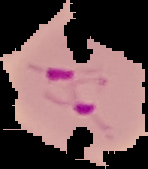 From a thin blood smear. Segmented cell region on a black background. Image is 148×169 pixels. Result: malaria parasites detected.